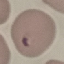

Summary:
  - Result: malaria parasites identified
  - Preparation: thin blood smear
  - Stain: Giemsa
  - Capture: smartphone through the microscope eyepiece
  - Image type: automatically extracted cell patch, resized to 64 × 64 pixels